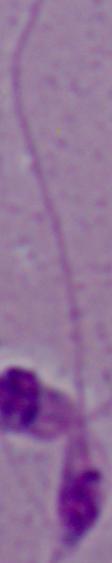 A Leishmania parasite is seen. 1000x magnification. Photomicrograph.